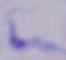

Summary:
  - Identification: trypanosome
  - Magnification: 1000x
  - Modality: micrograph